Name the blood parasite species.
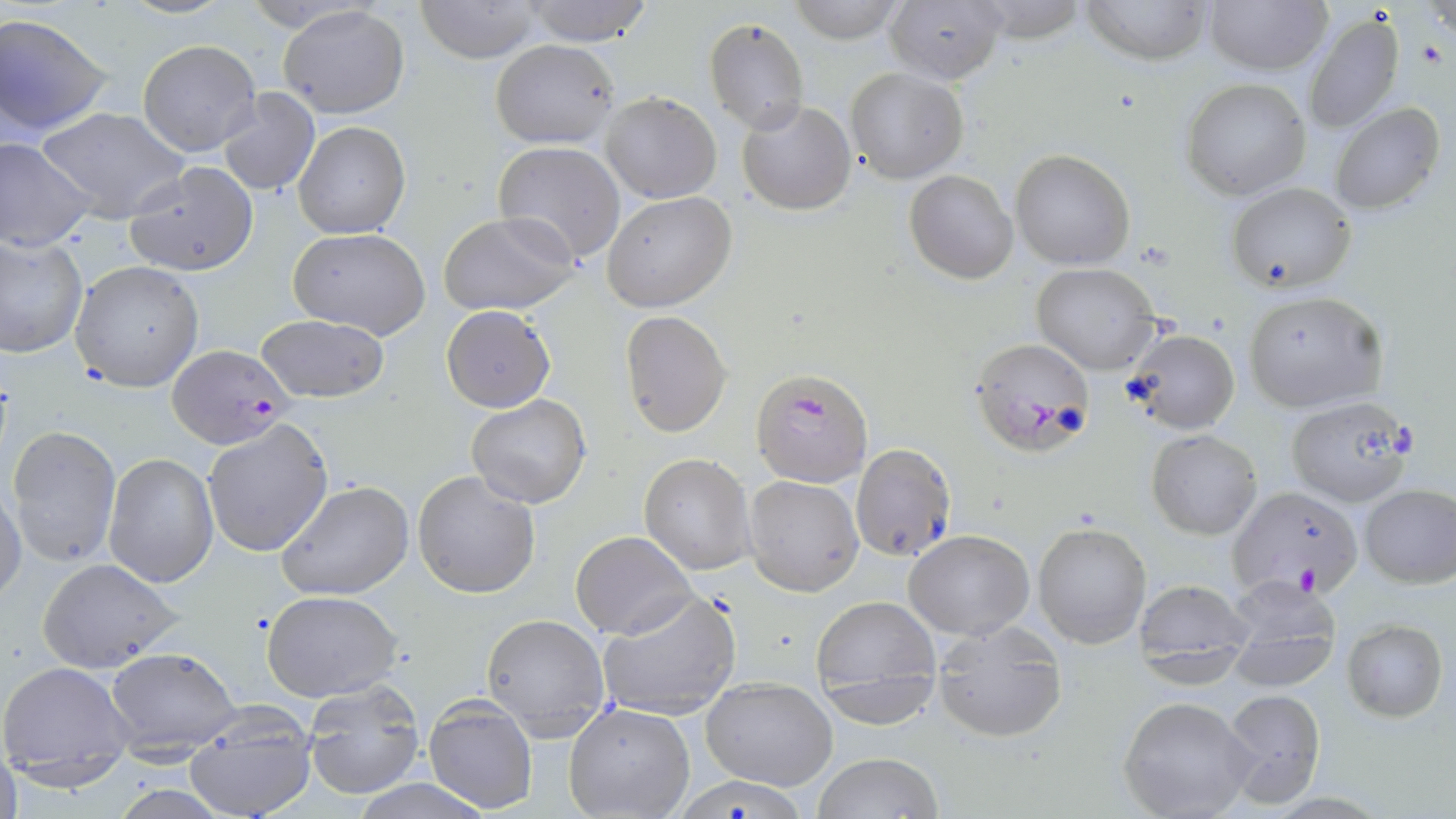
Plasmodium falciparum.

modality = optical microscopy
stain = May-Grünwald-Giemsa
magnification = 1000x
Plasmodium falciparum-infected red blood cell locations = approximate bounding boxes as (x1,y1)-(x2,y2) corner pairs in pixels: (970,336)-(1096,452), (167,345)-(293,450), (751,368)-(873,487), (1230,485)-(1364,599)
field of view = one of a larger specimen
preparation = thin blood film
uninfected red blood cell locations = approximate bounding boxes as (x1,y1)-(x2,y2) corner pairs in pixels: (115,0)-(237,20), (412,0)-(544,64), (519,0)-(658,46), (882,0)-(1007,85), (1079,0)-(1211,65), (784,1)-(911,44), (1203,1)-(1331,76), (279,4)-(408,119), (1,12)-(115,139), (1303,12)-(1405,134), (705,17)-(809,133), (138,38)-(261,157), (490,38)-(619,149), (845,68)-(969,183), (1181,78)-(1311,201), (216,87)-(321,196), (602,91)-(721,203), (738,99)-(857,214), (1329,102)-(1445,214), (36,107)-(191,223), (294,120)-(411,239), (0,136)-(96,252), (494,141)-(625,264), (1011,149)-(1134,270), (125,161)-(259,277), (904,170)-(1018,283), (1227,181)-(1357,293), (603,192)-(735,313), (438,211)-(579,313), (287,227)-(432,341), (0,236)-(88,357), (70,259)-(205,392), (1031,262)-(1163,375), (1243,289)-(1388,414), (441,305)-(556,413), (620,310)-(731,436), (255,313)-(389,404), (1126,328)-(1240,434), (466,396)-(593,509), (1285,396)-(1416,507), (201,420)-(332,558), (8,425)-(123,569), (1147,429)-(1263,540), (850,443)-(957,563), (638,452)-(756,575), (104,453)-(218,587), (412,471)-(541,599), (743,474)-(863,596), (276,480)-(414,602), (0,483)-(26,608), (1358,483)-(1455,587), (1032,521)-(1152,650), (904,530)-(1034,641), (571,531)-(695,641), (37,557)-(184,673), (1223,577)-(1344,693), (1131,578)-(1253,678), (260,589)-(405,702), (596,591)-(742,721), (811,592)-(941,700), (482,611)-(611,737), (1341,618)-(1448,723), (934,633)-(1070,742), (103,644)-(243,753), (2,661)-(138,784), (701,675)-(838,790), (302,678)-(425,800), (1222,687)-(1328,807), (1117,696)-(1260,819), (423,697)-(538,813), (564,703)-(694,819), (181,707)-(319,819), (0,743)-(22,819), (813,752)-(943,818), (670,776)-(814,819), (350,778)-(493,818)
image size = 1456×819 pixels